Name the blood parasite species.
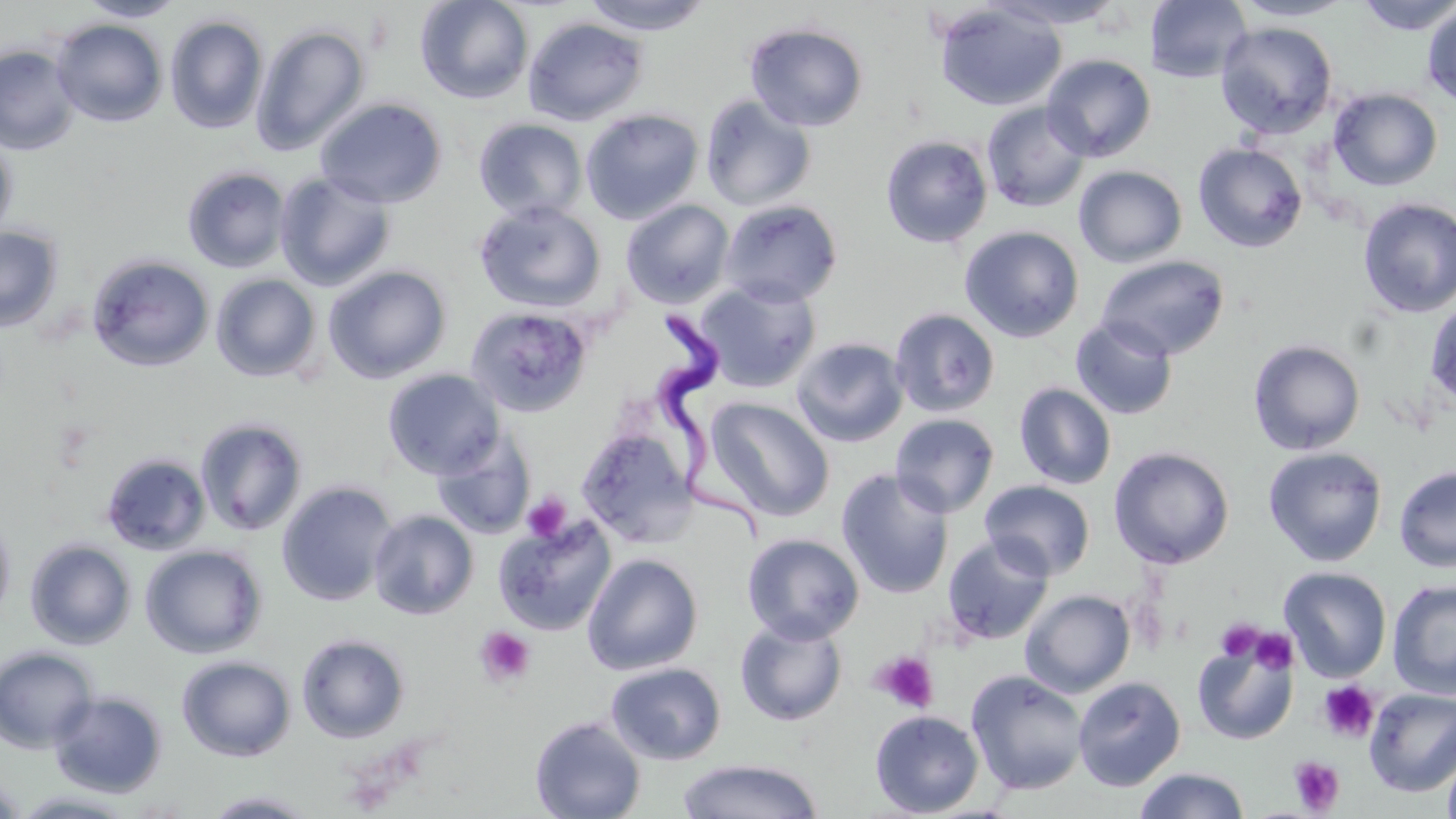

Trypanosoma brucei.

Summary:
  - Coordinate format: approximate bounding boxes as (x1,y1)-(x2,y2) corner pairs in pixels
  - Uninfected red blood cell locations: (76,0)-(188,22), (415,0)-(534,105), (579,0)-(716,35), (991,0)-(1127,29), (1149,0)-(1253,84), (1232,0)-(1355,21), (1356,0)-(1456,35), (934,2)-(1067,112), (1398,2)-(1453,78), (1421,4)-(1456,106), (165,14)-(269,134), (522,16)-(649,126), (51,18)-(168,127), (1215,21)-(1338,139), (744,22)-(869,131), (251,23)-(370,156), (0,44)-(80,156), (1041,54)-(1156,162), (1329,88)-(1443,191), (699,94)-(817,212), (316,97)-(447,208), (981,101)-(1091,213), (581,109)-(704,224), (474,118)-(588,221), (0,131)-(18,243), (880,134)-(993,248), (1192,142)-(1308,253), (1073,165)-(1188,268), (182,166)-(291,273), (274,171)-(397,291), (1357,198)-(1456,318), (621,199)-(735,308), (719,199)-(843,307), (473,200)-(607,314), (959,225)-(1084,343), (0,226)-(63,332), (87,254)-(215,372), (1095,254)-(1230,360), (323,266)-(451,383), (211,273)-(322,382), (695,280)-(821,393), (1425,295)-(1456,414), (466,305)-(593,418), (889,307)-(1000,418), (1071,316)-(1179,420), (790,337)-(909,448), (1248,339)-(1366,455), (382,368)-(505,479), (1014,382)-(1117,490), (706,397)-(835,520), (890,413)-(1000,518), (194,417)-(309,536), (577,426)-(698,547), (432,430)-(535,539), (1108,446)-(1234,570), (1263,446)-(1387,566), (101,451)-(211,556), (1393,465)-(1456,572), (836,468)-(954,599), (979,480)-(1095,580), (276,481)-(399,607), (0,509)-(16,630), (369,509)-(479,620), (494,515)-(616,636), (741,533)-(865,644), (942,534)-(1054,646), (24,539)-(136,650), (140,544)-(267,659), (582,554)-(703,675), (1279,566)-(1392,682), (1387,579)-(1456,700), (1020,589)-(1135,697), (734,617)-(847,727), (296,633)-(410,744), (1192,634)-(1299,746), (0,646)-(99,754), (176,655)-(296,762), (605,662)-(727,765), (965,669)-(1089,796), (1073,676)-(1186,791), (1364,688)-(1456,797), (48,690)-(168,798), (869,710)-(984,817), (529,716)-(646,819), (1442,746)-(1456,819), (676,758)-(824,818), (1133,767)-(1251,819), (0,773)-(25,819), (11,790)-(139,818), (201,790)-(320,818)
  - Platelet locations: (522,491)-(571,543), (1216,619)-(1263,662), (474,626)-(536,688), (1250,629)-(1297,674), (871,651)-(939,714), (1317,681)-(1380,742), (1289,756)-(1345,815)
  - Trypanosoma brucei locations: (654,313)-(783,545)
  - Field of view: single
  - Image size: 1456×819 pixels
  - Preparation: thin blood smear
  - Stain: May-Grünwald-Giemsa
  - Magnification: 1000x
  - Modality: optical microscopy